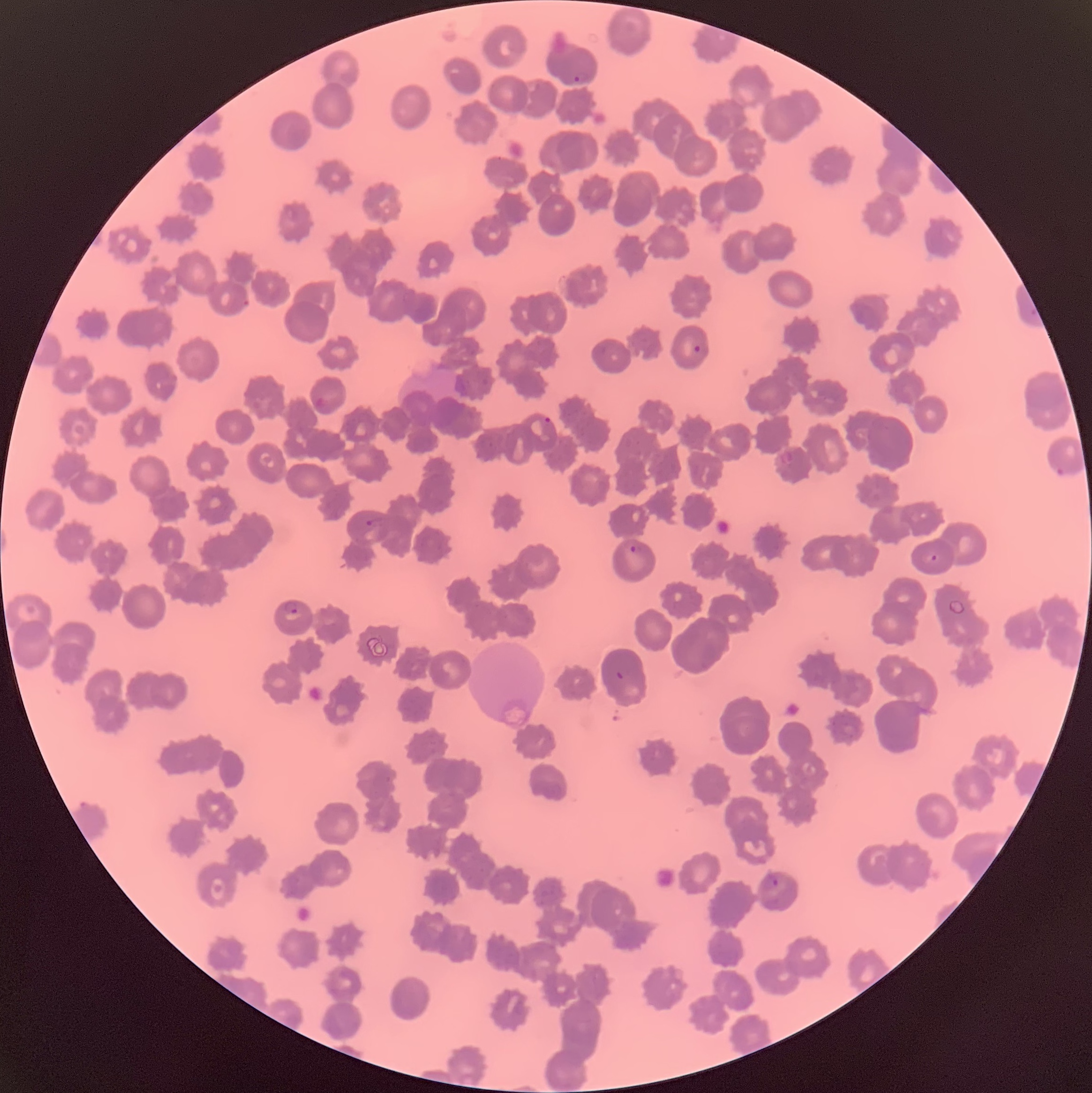
Approximate bounding boxes as [x1, y1, x2, y2] in pixels. Plasmodium parasite locations: [574, 72, 593, 83], [693, 343, 705, 359], [543, 417, 553, 424], [1054, 465, 1064, 476], [365, 518, 384, 527], [630, 543, 643, 555], [283, 601, 299, 614], [616, 671, 625, 680], [762, 874, 778, 891]. Plasmodium parasites too small for a box (approximate centers as [x, y] in pixels): [934, 557]. Light microscopy. Image is 1092×1093 pixels. The red blood cells show rouleaux formation. Thin blood smear.